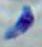 1000x magnification. Photomicrograph. Toxoplasma gondii is shown.